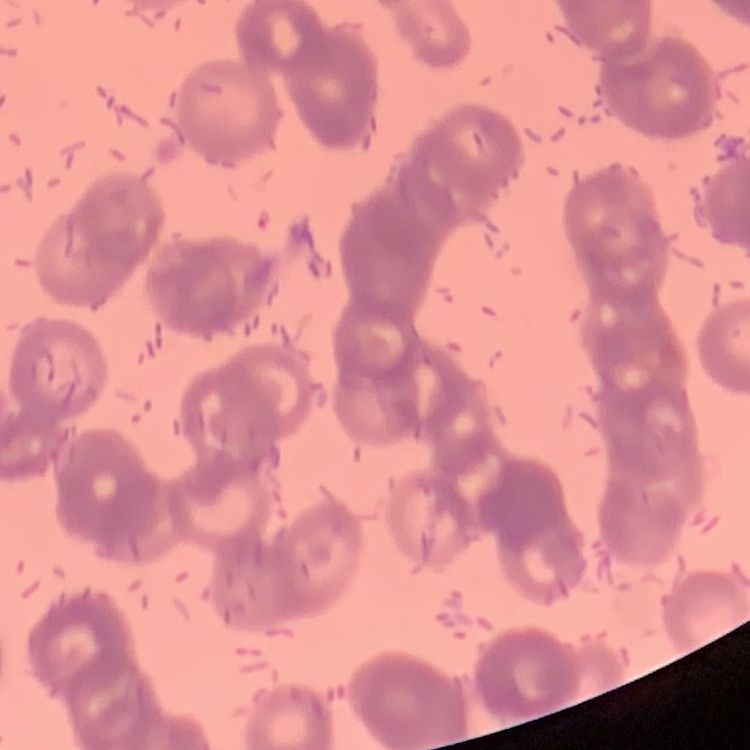
Summary:
  - Red blood cell morphology: rouleaux formation
  - Stain: Field's or Giemsa
  - Image type: square crop of a larger photomicrograph
  - Preparation: thin blood smear